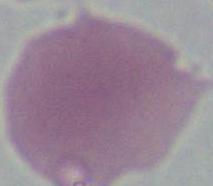
Summary:
  - Modality: photomicrograph
  - Identification: erythrocyte
  - Magnification: 1000x